Locate leukocytes (white blood cells).
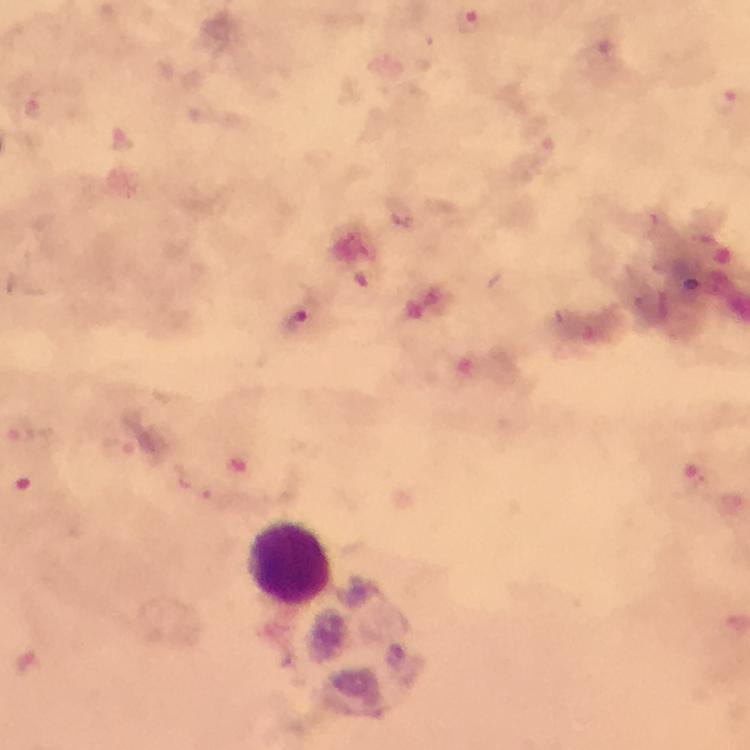

Approximate object centers, in pixels from the top-left corner.
Leukocytes: (x=292, y=566).

Summary:
  - Plasmodium parasite locations: (x=298, y=319), (x=22, y=434), (x=693, y=481)
  - Image size: 750×750 pixels
  - Cropped from: one field of view
  - Context: from a diagnostic examination for malaria
  - Magnification: 100x
  - Stain: Giemsa
  - Capture: smartphone mounted on the microscope
  - Preparation: thick blood film
  - Immersion oil: applied